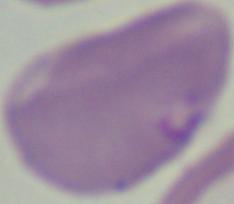

magnification: 1000x
modality: photomicrograph
identification: Babesia